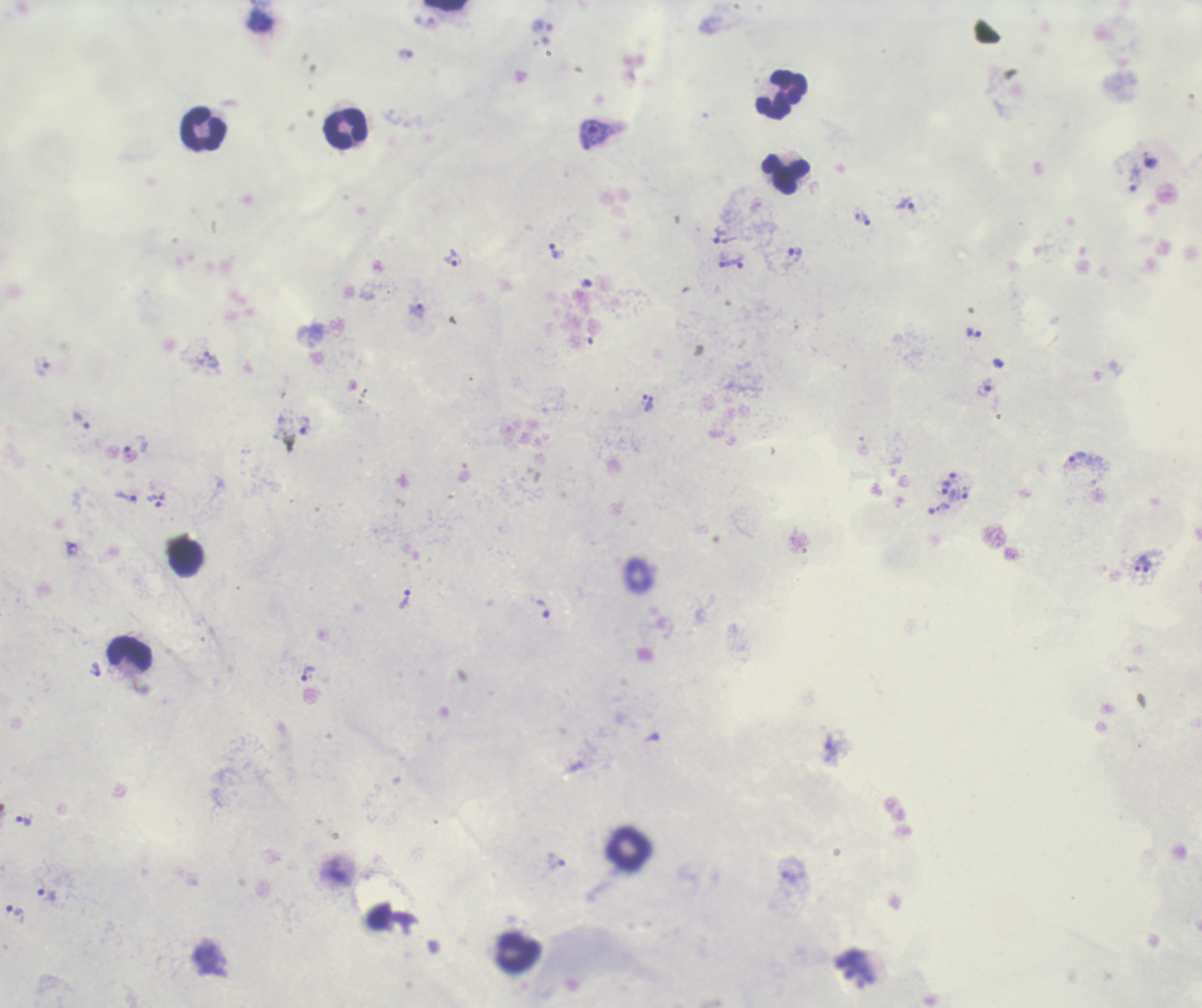

coordinate format = approximate object centers, in pixels from the top-left corner
trophozoite locations = (x=594, y=135), (x=906, y=204), (x=865, y=220), (x=719, y=235), (x=555, y=252), (x=795, y=252), (x=453, y=259), (x=739, y=262), (x=724, y=264), (x=416, y=310), (x=974, y=333), (x=984, y=388), (x=649, y=403), (x=82, y=421), (x=305, y=427), (x=1078, y=458), (x=946, y=487), (x=959, y=495), (x=127, y=497), (x=939, y=509), (x=1139, y=564), (x=1147, y=567), (x=405, y=599), (x=543, y=610), (x=96, y=670), (x=307, y=673), (x=24, y=822), (x=556, y=865), (x=48, y=895), (x=15, y=914)
leukocyte locations = (x=446, y=5), (x=781, y=94), (x=203, y=128), (x=346, y=128), (x=785, y=173), (x=186, y=559), (x=128, y=652), (x=518, y=953)
context = previously used in an actual diagnosis
coloration quality = good
field of view = one from this slide
result = Plasmodium parasites identified
stain = Romanowsky
preparation = thick smear of blood
magnification = 100x
image size = 1202×1008 pixels
background quality = good